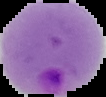

Malaria status: parasitized. Image is 106×97 pixels. The area outside the segmented cell region is set to black. From a thin blood film.